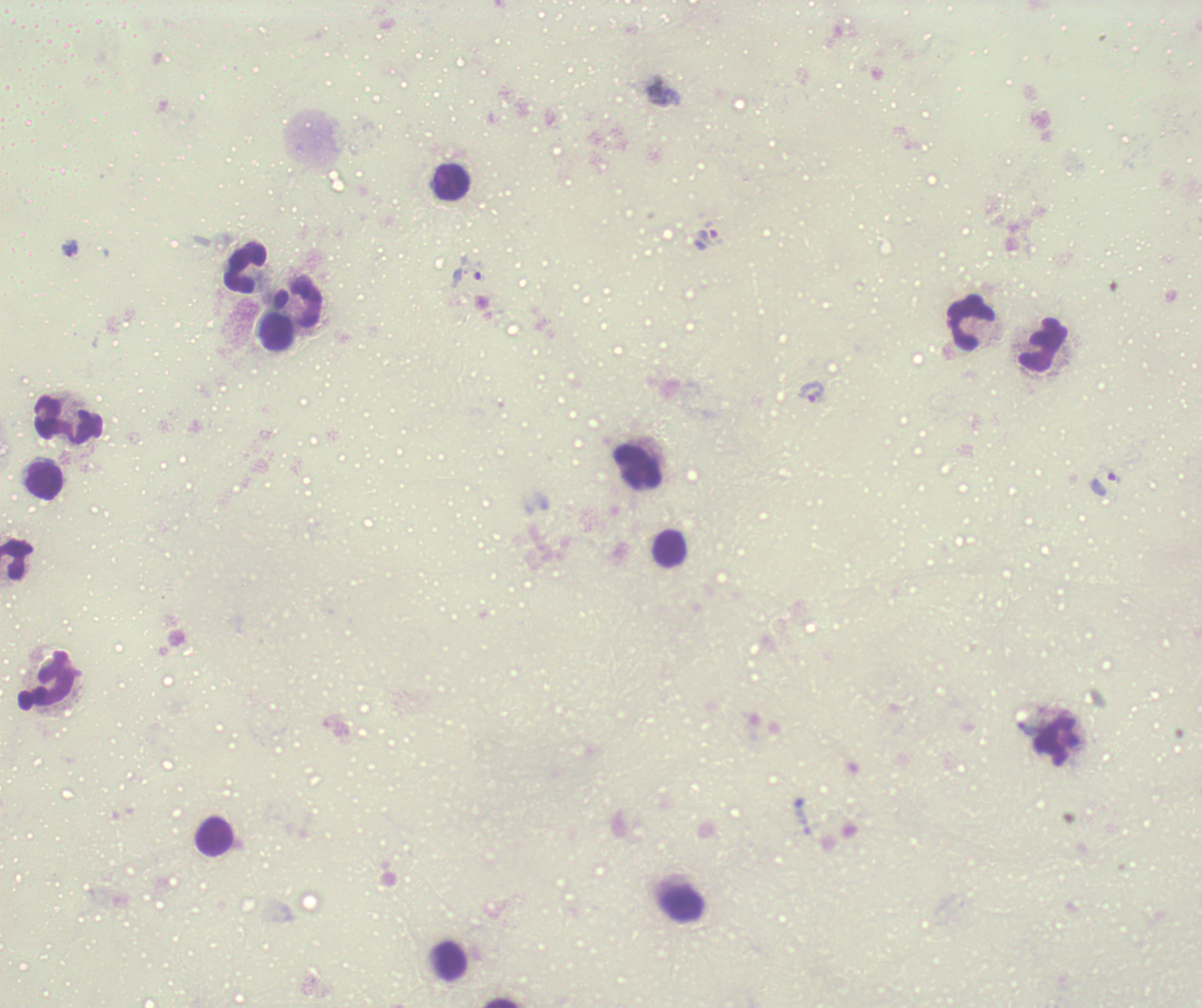
coordinate format = approximate object centers, in pixels from the top-left corner
leukocyte locations = (x=452, y=181), (x=246, y=268), (x=297, y=303), (x=971, y=324), (x=276, y=331), (x=1043, y=345), (x=68, y=421), (x=637, y=467), (x=44, y=480), (x=669, y=549), (x=16, y=559), (x=47, y=680), (x=1057, y=743), (x=214, y=836), (x=682, y=904), (x=450, y=961), (x=503, y=1003)
trophozoite locations = (x=712, y=237), (x=70, y=249), (x=467, y=273), (x=813, y=392), (x=1105, y=481), (x=1029, y=729)
result = malaria parasites detected
field of view = one from this slide
context = previously used in a real diagnosis
image size = 1202×1008 pixels
magnification = 100x
background quality = unsatisfactory
stain = Romanowsky
preparation = thick blood smear
coloration quality = bad